Identify the parasite.
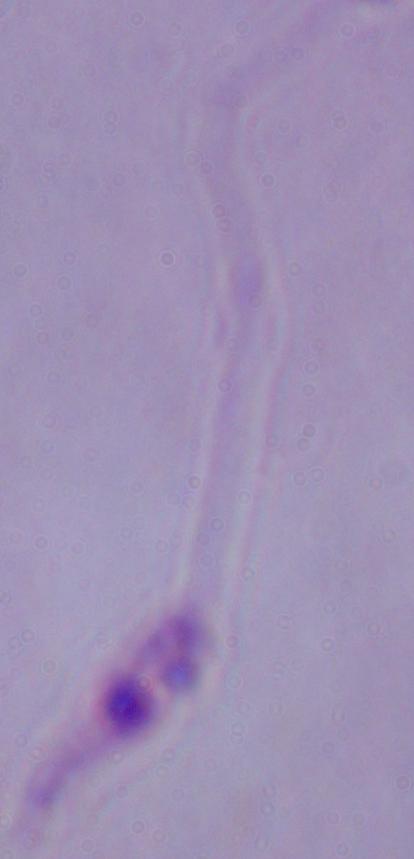
This is Leishmania.

modality = photomicrograph
magnification = 1000x